Name the blood parasite species.
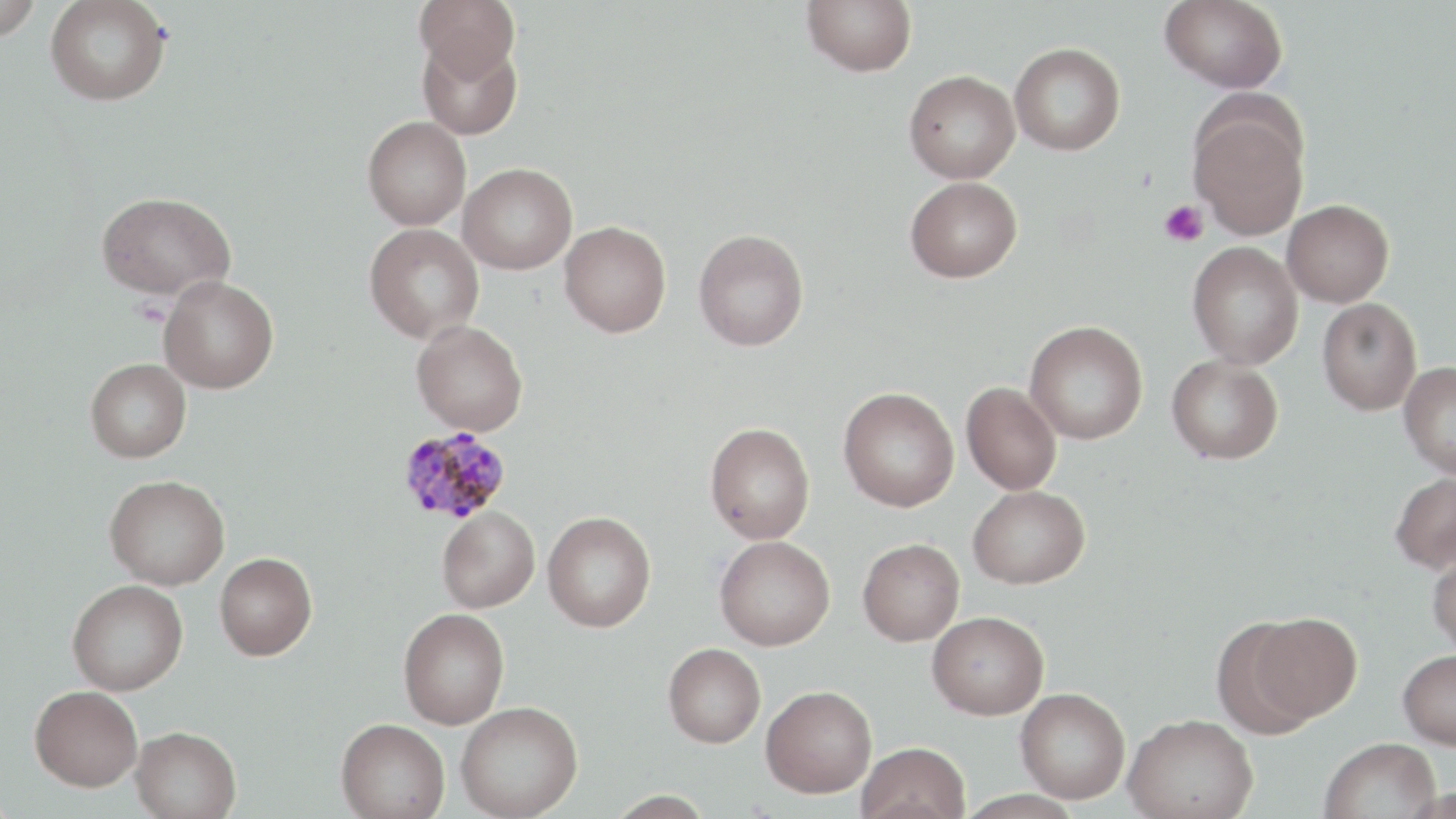
Plasmodium malariae.

image size = 1456×819 pixels
Plasmodium malariae-infected red blood cell locations = approximate bounding boxes as (x1,y1)-(x2,y2) corner pairs in pixels: (397,426)-(513,524)
uninfected red blood cell locations = approximate bounding boxes as (x1,y1)-(x2,y2) corner pairs in pixels: (0,0)-(42,40), (415,0)-(520,82), (802,0)-(917,76), (1160,0)-(1289,93), (45,1)-(172,105), (417,36)-(522,140), (1009,42)-(1126,156), (904,70)-(1020,183), (1189,106)-(1309,239), (362,116)-(471,230), (458,162)-(578,274), (905,176)-(1022,283), (96,190)-(235,301), (1282,199)-(1394,307), (559,220)-(672,337), (364,223)-(484,344), (693,229)-(809,351), (1187,241)-(1303,369), (159,274)-(279,393), (1317,297)-(1422,415), (411,320)-(528,435), (1024,320)-(1148,444), (1167,354)-(1283,464), (85,359)-(191,462), (1399,360)-(1456,479), (961,382)-(1062,495), (838,386)-(959,512), (704,422)-(815,544), (1390,471)-(1456,574), (105,475)-(229,590), (968,485)-(1089,588), (437,506)-(540,612), (542,511)-(656,632), (714,535)-(835,650), (858,538)-(964,646), (1427,546)-(1456,657), (214,551)-(318,659), (67,579)-(188,695), (398,608)-(509,729), (927,610)-(1050,719), (1247,611)-(1363,723), (1211,619)-(1318,740), (663,643)-(766,747), (1398,650)-(1456,749), (30,685)-(143,791), (761,685)-(877,797), (1016,688)-(1130,803), (456,701)-(583,819), (1124,712)-(1259,819), (336,718)-(450,818), (131,725)-(242,819), (1320,737)-(1440,819), (856,741)-(970,819), (603,790)-(716,817)
field of view = one of a larger specimen
modality = optical microscopy
preparation = thin blood smear
stain = May-Grünwald-Giemsa
platelet locations = approximate bounding boxes as (x1,y1)-(x2,y2) corner pairs in pixels: (1160,200)-(1208,247)
magnification = 1000x